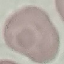 Result: no malaria parasites detected. Automatically extracted cell patch, resized to 64 × 64 pixels. Giemsa stain. Thin blood smear. Photographed with a smartphone camera at the microscope eyepiece.